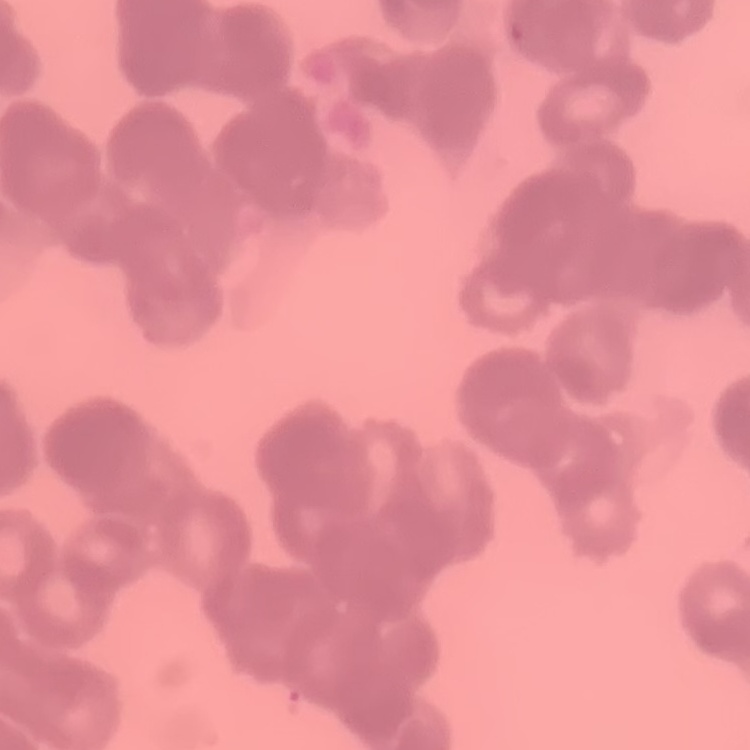
red_blood_cell_morphology: rouleaux formation
stain: Field's or Giemsa
image_type: square crop of a larger photomicrograph
preparation: thin blood film